Identify the preparation type.
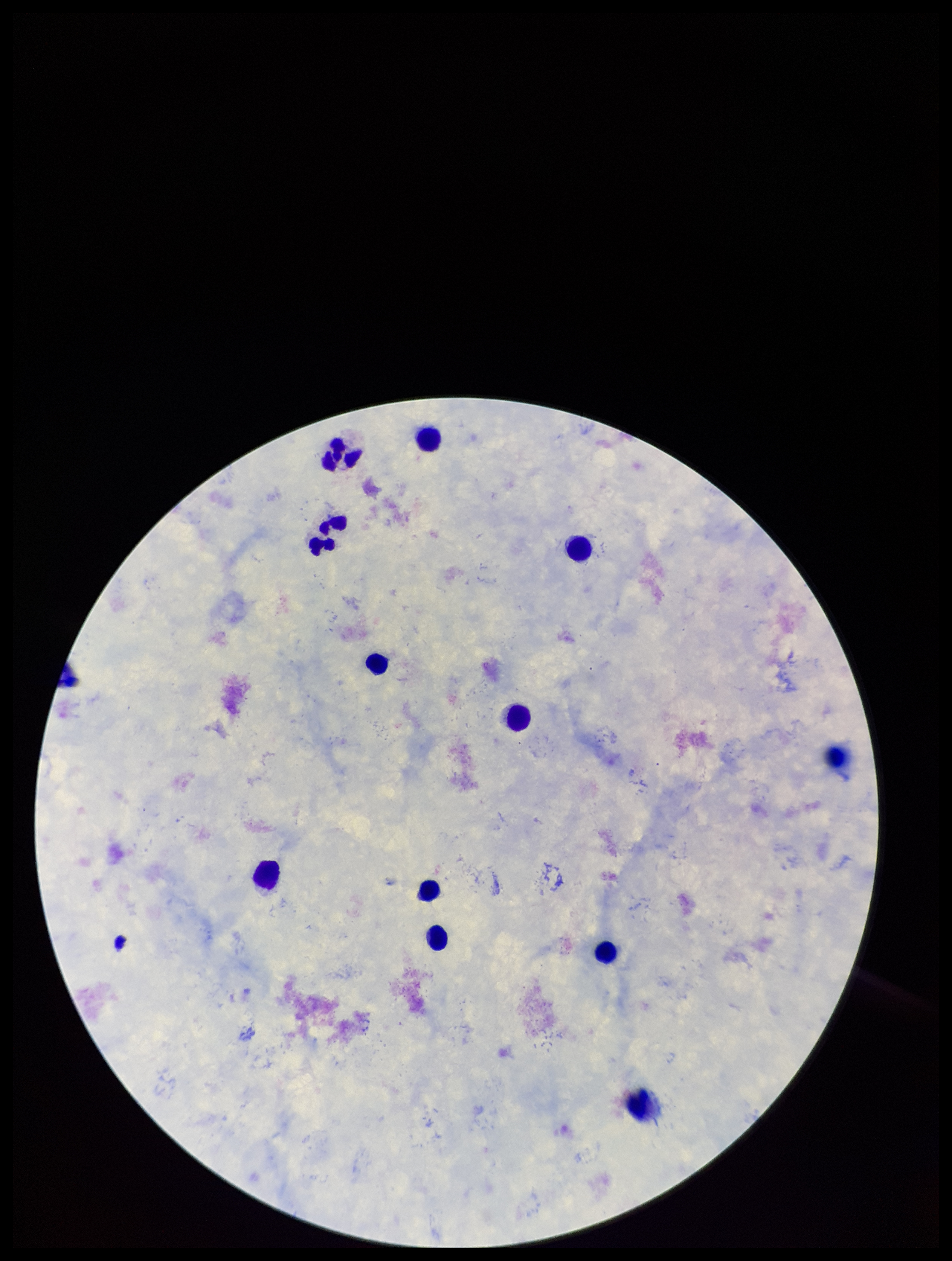

Thick.

Summary:
  - Field of view: single
  - Plasmodium parasites: none detected
  - Image size: 952×1261 pixels
  - Stain: Giemsa
  - Leukocyte count: 13
  - Parasite count: 0
  - Capture: smartphone photograph through the microscope eyepiece
  - Patient malaria status: negative